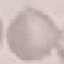
Summary:
  - Result: no malaria parasites seen
  - Stain: Giemsa
  - Image type: automatically extracted cell patch, resized to 64 × 64 pixels
  - Capture: smartphone through the microscope eyepiece
  - Preparation: thin blood film